Evaluate for malaria.
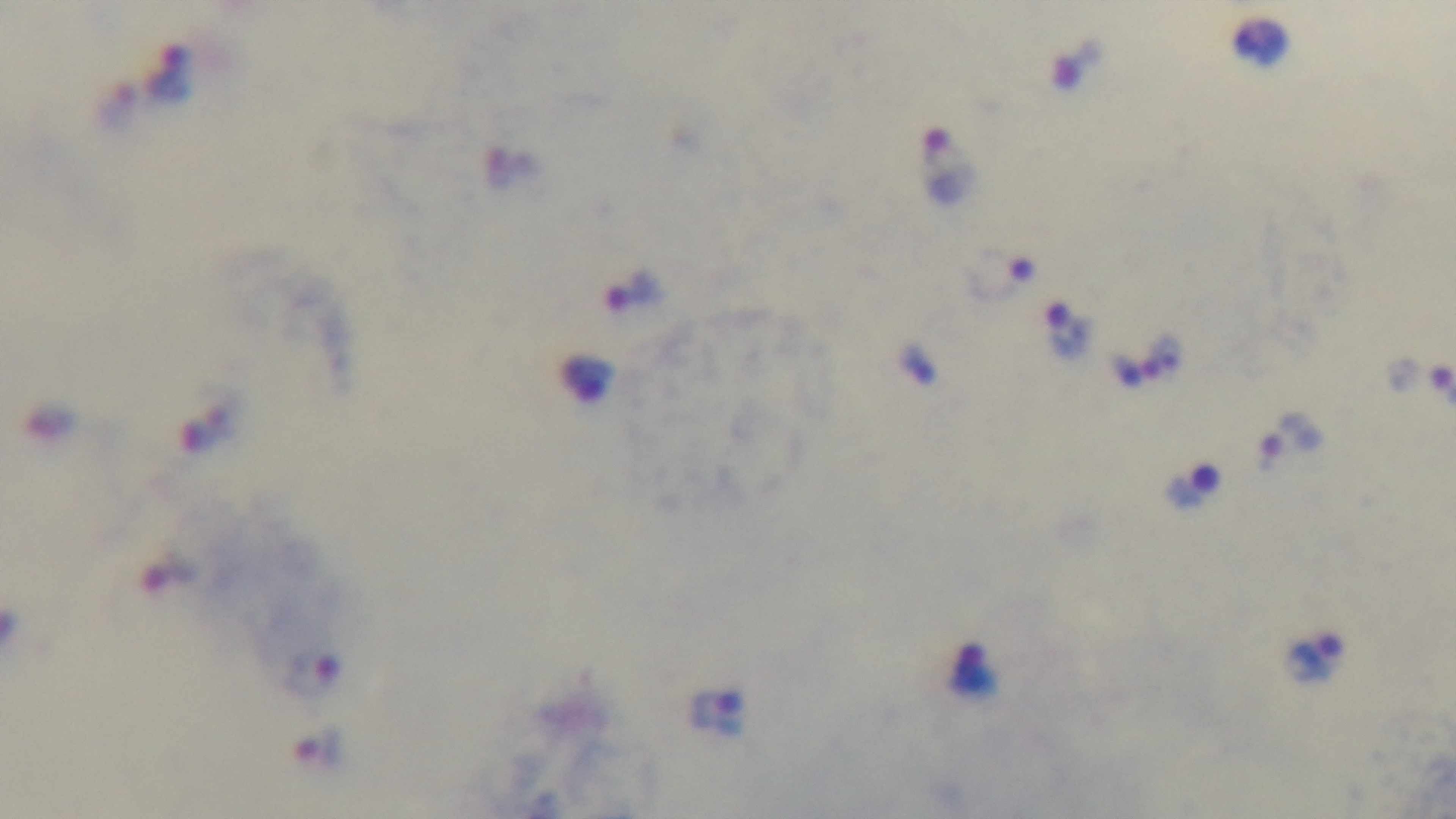

Infected.

Giemsa stain. Photomicrograph. Preparation: thick blood film. Single field of view. Captured with a mounted 4K digital camera. 100x oil-immersion objective.